Report the malaria status of this cell.
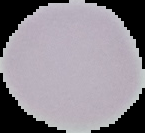

Uninfected.

Summary:
  - Image size: 145×133 pixels
  - Image type: cell region segmented out of the field of view; surrounding area masked to black
  - Preparation: thin blood smear